Classify this cell by malaria status.
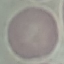

Uninfected.

Acquired by smartphone through the microscope eyepiece. Thin smear of blood. Giemsa stain. Cell patch, automatically extracted from a larger field of view and resized to 64 × 64 pixels.